Assess the morphology of the erythrocytes.
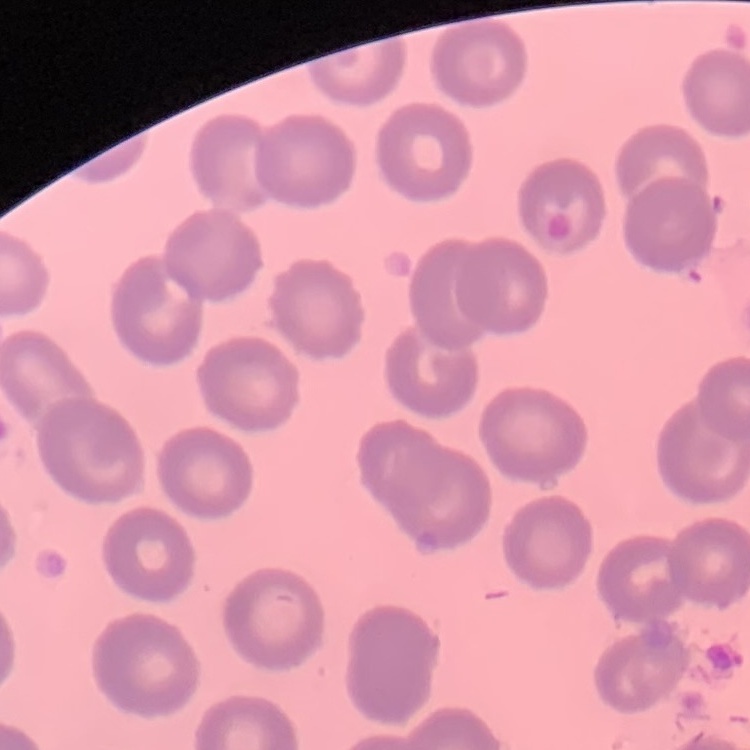
No rouleaux formation.

image type = one tile cut from a larger photomicrograph
stain = Field's or Giemsa
preparation = thin blood smear